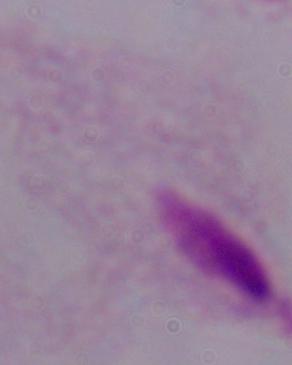
Summary:
  - Modality: micrograph
  - Identification: trichomonad
  - Magnification: 1000x